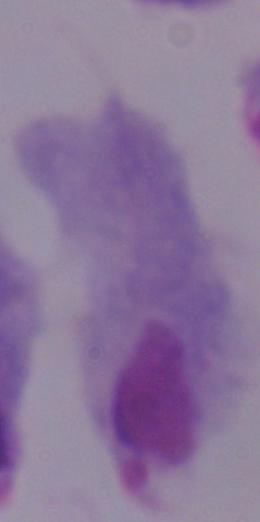
Summary:
  - Identification: trichomonad
  - Modality: micrograph
  - Magnification: 1000x